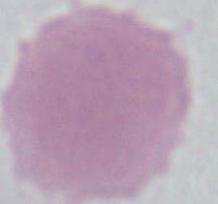
modality = micrograph
identification = erythrocyte
magnification = 1000x